State which parasite is depicted.
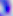

This is Toxoplasma gondii.

modality: micrograph
magnification: 400x